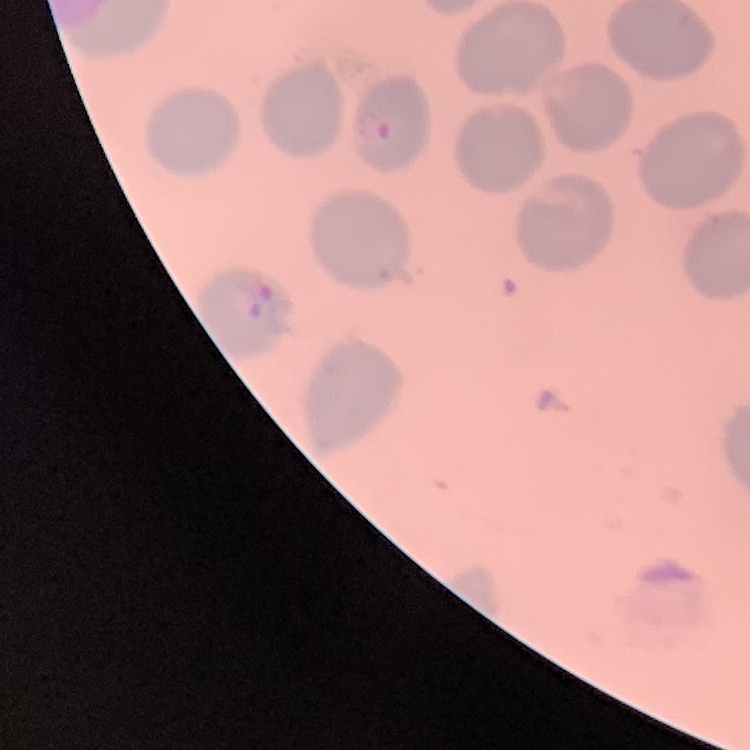

The red blood cells show no rouleaux formation. Field's or Giemsa stain. Thin blood film. Square crop of a larger photomicrograph.